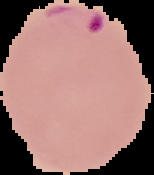

Malaria status: parasitized. From a thin blood smear. Segmented cell region on a black background. Image is 154×175 pixels.